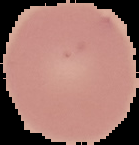

From a thin blood film. Result: no Plasmodium parasites detected. Segmented cell region on a black background. Image is 139×145 pixels.